Classify this cell by malaria status.
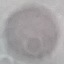

It is uninfected.

Summary:
  - Stain: Giemsa
  - Capture: smartphone through the microscope eyepiece
  - Image type: automatically extracted cell patch, resized to 64 × 64 pixels
  - Preparation: thin blood film